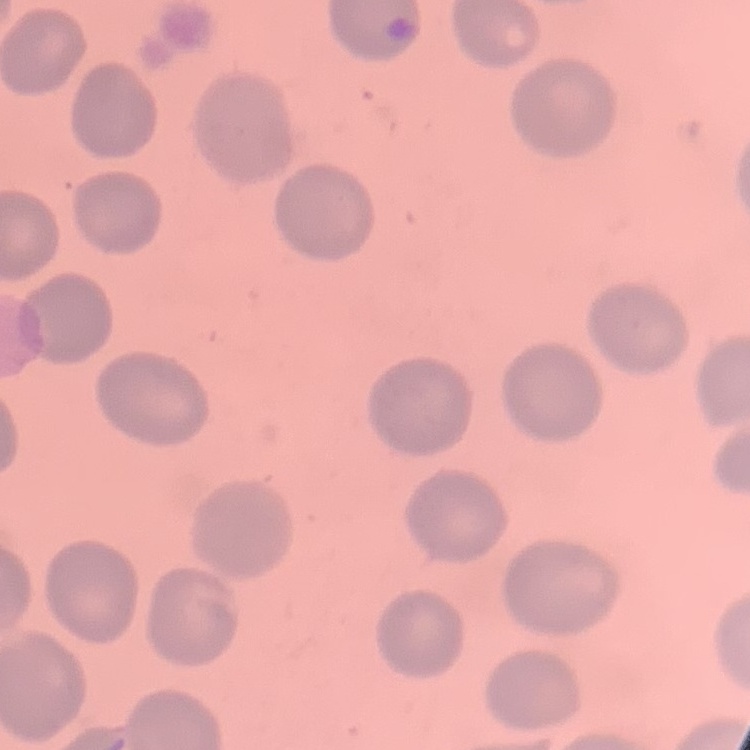
Summary:
  - Erythrocyte morphology: no rouleaux formation
  - Preparation: thin blood film
  - Stain: Field's or Giemsa
  - Image type: one tile cut from a larger photomicrograph